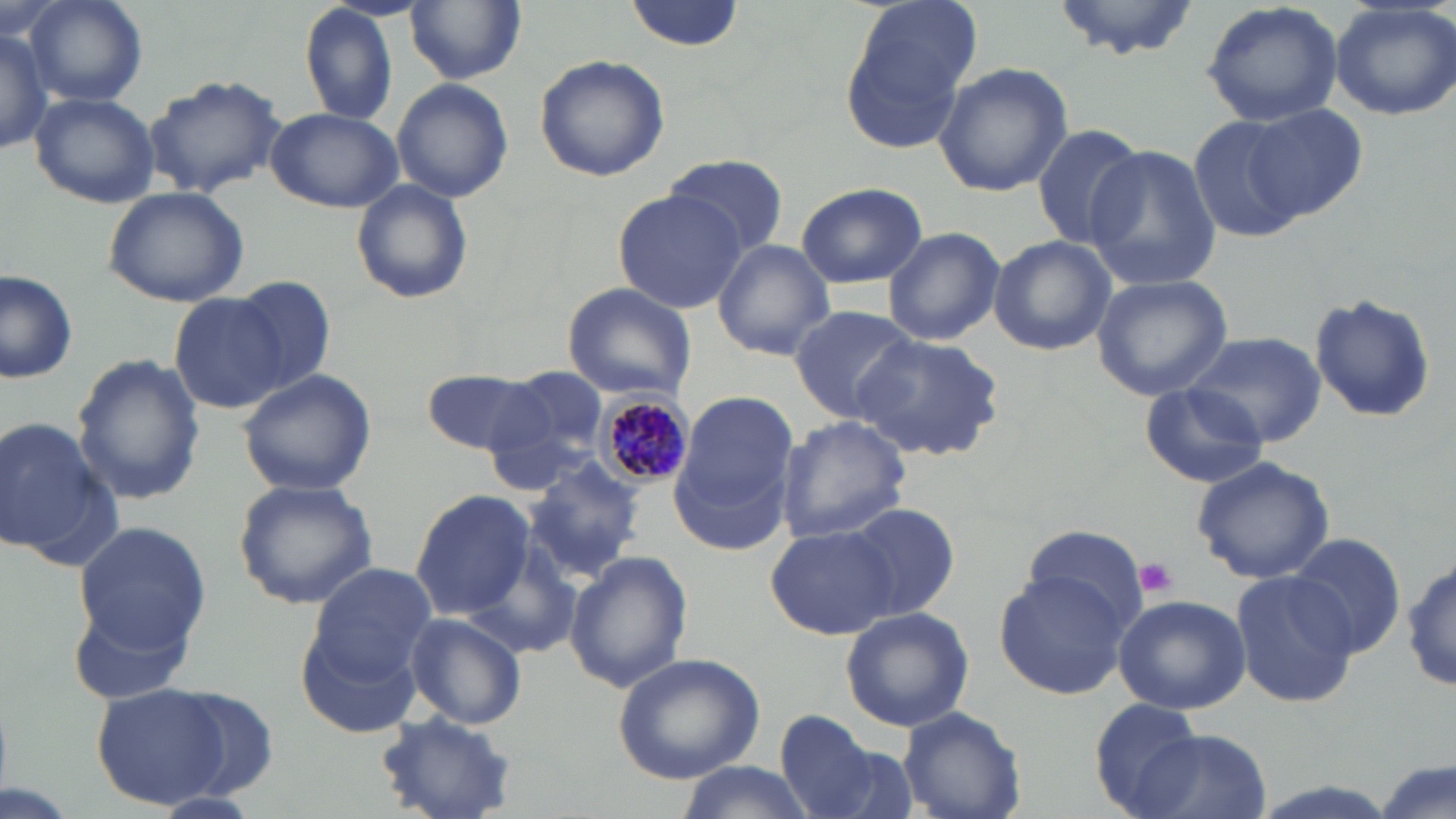
{
  "plasmodium_malariae_infected_red_blood_cell_locations": "approximate bounding boxes as [x1, y1, x2, y2] in pixels: [596, 391, 695, 486]",
  "slide_level_diagnosis": "Plasmodium malariae",
  "modality": "light microscopy",
  "magnification": "1000x",
  "uninfected_red_blood_cell_locations": "approximate bounding boxes as [x1, y1, x2, y2] in pixels: [23, 0, 148, 108], [625, 0, 744, 51], [1051, 0, 1207, 62], [1200, 0, 1344, 128], [297, 1, 398, 127], [405, 1, 526, 85], [1328, 1, 1456, 122], [840, 4, 977, 154], [0, 24, 51, 156], [534, 55, 670, 181], [933, 62, 1073, 197], [143, 73, 287, 197], [391, 78, 513, 204], [29, 91, 160, 208], [1243, 104, 1371, 222], [266, 108, 403, 213], [1191, 116, 1308, 244], [1030, 123, 1146, 248], [1082, 145, 1223, 291], [661, 152, 790, 258], [350, 178, 471, 302], [796, 182, 927, 289], [102, 186, 251, 307], [612, 191, 747, 313], [882, 226, 1004, 346], [987, 235, 1115, 356], [712, 239, 835, 360], [738, 240, 883, 409], [0, 267, 79, 387], [1090, 274, 1234, 402], [228, 277, 337, 396], [559, 283, 696, 402], [171, 292, 291, 413], [1307, 292, 1438, 427], [789, 305, 921, 421], [1185, 332, 1326, 447], [852, 335, 1005, 461], [72, 352, 205, 505], [238, 369, 377, 498], [424, 369, 550, 454], [506, 370, 611, 461], [1141, 380, 1270, 489], [676, 392, 798, 518], [0, 415, 112, 567], [775, 415, 912, 542], [524, 455, 648, 582], [1191, 456, 1334, 583], [232, 478, 379, 611], [411, 489, 536, 621], [839, 502, 960, 624], [74, 519, 212, 654], [1013, 522, 1148, 642], [765, 524, 898, 639], [1288, 534, 1405, 660], [460, 542, 585, 662], [563, 551, 694, 692], [1406, 556, 1454, 695], [305, 560, 437, 681], [995, 566, 1134, 699], [1229, 567, 1362, 709], [1113, 593, 1250, 715], [68, 598, 197, 706], [840, 607, 974, 733], [405, 612, 527, 728], [295, 616, 426, 741], [611, 651, 767, 784], [92, 681, 232, 809], [164, 686, 284, 799], [1088, 698, 1210, 816], [896, 706, 1026, 819], [778, 711, 883, 816], [375, 714, 522, 817], [1140, 730, 1272, 819], [1375, 757, 1453, 819], [673, 764, 819, 818]",
  "platelet_locations": "approximate bounding boxes as [x1, y1, x2, y2] in pixels: [1134, 558, 1178, 600]",
  "stain": "May-Grünwald-Giemsa",
  "field_of_view": "one of a larger specimen",
  "preparation": "thin blood film",
  "image_size": "1456×819 pixels"
}